Assess this cell for malaria.
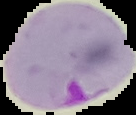
Parasitized.

Image is 136×115 pixels. Segmented cell region on a black background. From a thin blood smear.